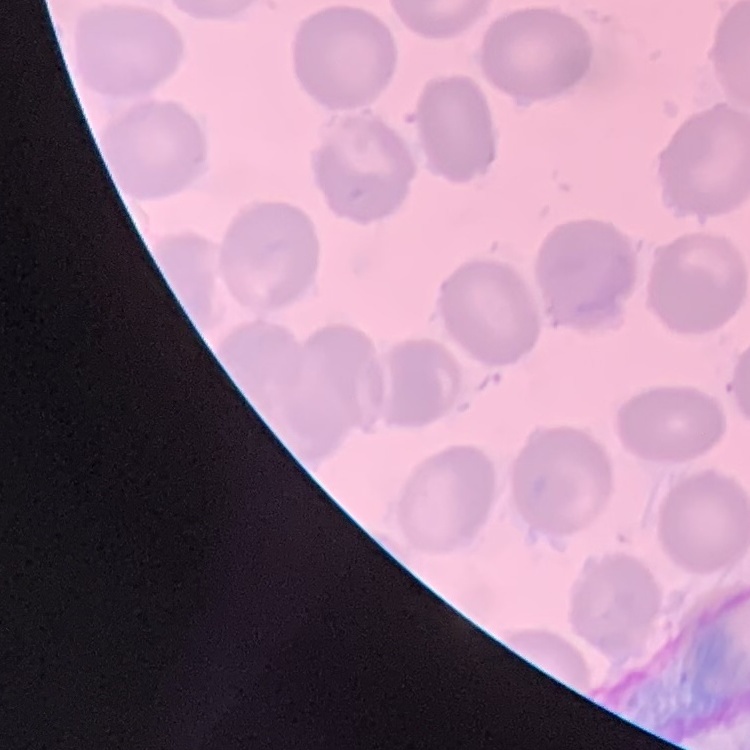
The erythrocytes show no rouleaux formation. Stained with either Field's or Giemsa. Square crop of a larger photomicrograph. Thin blood smear.